Name the blood parasite species.
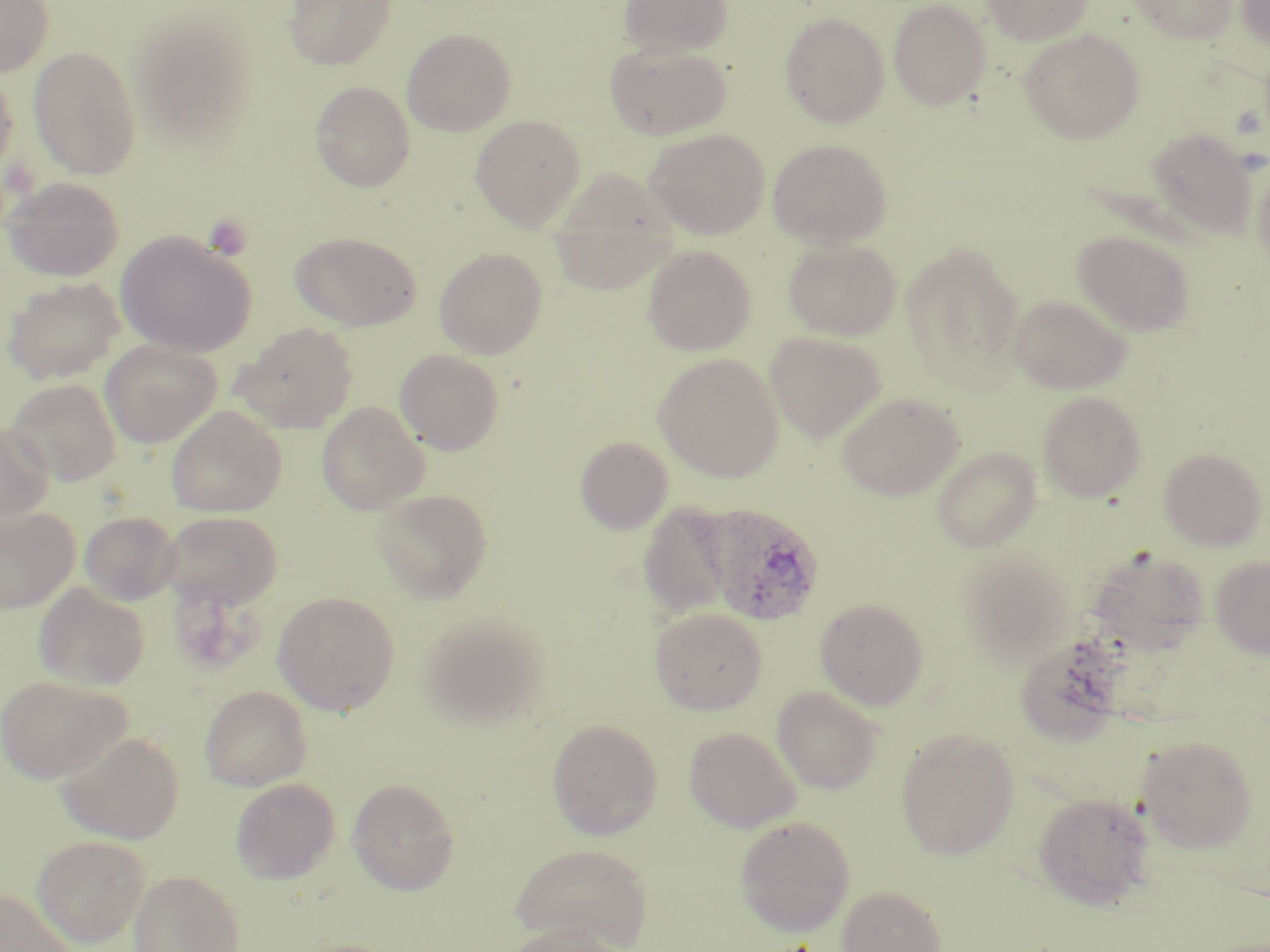

Plasmodium ovale.

{
  "stain": "May-Grünwald-Giemsa",
  "field_of_view": "one of a larger specimen",
  "plasmodium_ovale_infected_red_blood_cell_locations": "approximate bounding boxes as (x1,y1)-(x2,y2) corner pairs in pixels: (701,503)-(825,626)",
  "uninfected_red_blood_cell_locations": "approximate bounding boxes as (x1,y1)-(x2,y2) corner pairs in pixels: (0,0)-(54,77), (283,0)-(398,71), (617,0)-(733,58), (982,0)-(1093,46), (1128,0)-(1240,44), (1236,0)-(1270,54), (887,1)-(992,110), (780,11)-(890,128), (128,13)-(257,145), (401,28)-(516,136), (1018,29)-(1145,144), (605,41)-(730,141), (28,46)-(142,179), (0,68)-(19,182), (309,81)-(416,193), (470,114)-(587,230), (644,128)-(769,239), (1146,129)-(1257,238), (768,139)-(893,246), (1251,157)-(1270,276), (2,176)-(124,281), (548,184)-(680,299), (1072,230)-(1195,336), (116,232)-(256,358), (290,232)-(421,331), (783,238)-(902,341), (901,241)-(1027,394), (642,244)-(755,355), (434,247)-(548,359), (1,277)-(126,386), (1009,294)-(1133,394), (233,322)-(359,433), (764,331)-(887,444), (100,339)-(222,448), (395,349)-(504,455), (653,354)-(784,482), (5,378)-(123,486), (1036,390)-(1146,502), (836,392)-(964,501), (317,401)-(430,514), (166,405)-(287,517), (0,421)-(54,526), (575,436)-(673,535), (931,447)-(1042,553), (1158,447)-(1267,550), (372,487)-(493,603), (637,502)-(737,619), (0,506)-(80,613), (79,511)-(181,606), (159,511)-(282,609), (1086,546)-(1211,653), (958,547)-(1077,667), (1211,555)-(1270,659), (33,582)-(150,691), (272,590)-(401,714), (815,597)-(929,709), (650,607)-(767,715), (417,612)-(550,731), (1013,634)-(1128,746), (0,675)-(129,784), (199,685)-(312,791), (772,686)-(883,794), (547,718)-(664,840), (684,726)-(800,833), (895,726)-(1020,859), (56,730)-(185,845), (1135,733)-(1258,852), (230,777)-(340,884), (347,777)-(460,895), (1033,792)-(1156,909), (734,815)-(855,937), (31,835)-(149,947), (510,843)-(653,950), (129,869)-(245,952), (836,884)-(947,952), (0,889)-(78,952), (504,922)-(626,952)",
  "modality": "optical microscopy",
  "preparation": "thin blood film",
  "platelet_locations": "approximate bounding boxes as (x1,y1)-(x2,y2) corner pairs in pixels: (203,214)-(253,260)",
  "magnification": "1000x",
  "image_size": "1270×952 pixels"
}